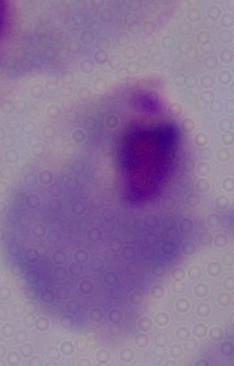

{
  "modality": "micrograph",
  "identification": "trichomonad",
  "magnification": "1000x"
}